Assess this cell for malaria.
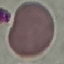

Uninfected.

Giemsa stain. Acquired by smartphone through the microscope eyepiece. Thin blood film. Automatically extracted cell patch, resized to 64 × 64 pixels.